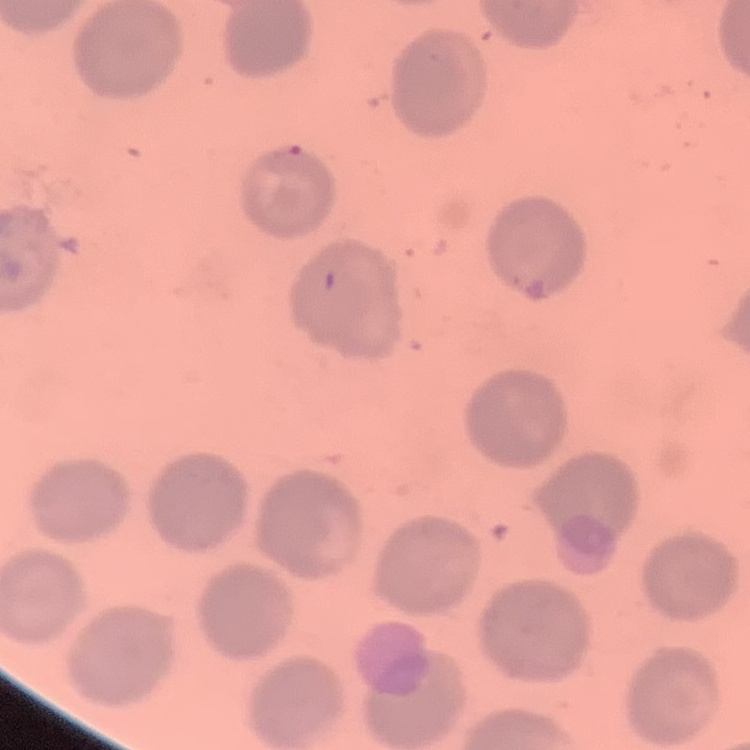

The red blood cells show no rouleaux formation. Thin blood film. Square crop of a larger photomicrograph. Field's or Giemsa stain.